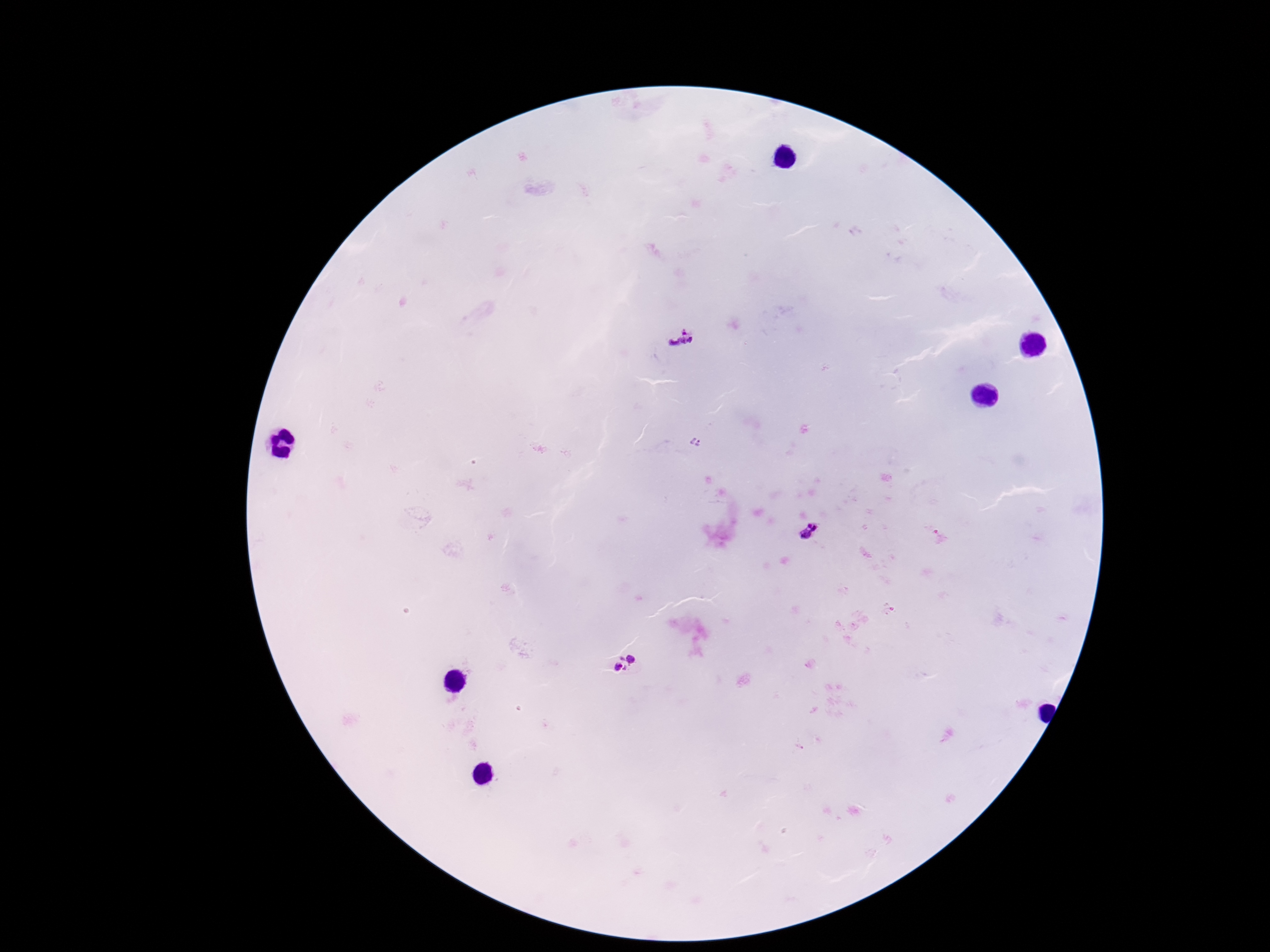

capture = smartphone camera through the microscope eyepiece
patient malaria status = positive
image size = 1270×952 pixels
magnification = 100x
field of view = one from this slide
Plasmodium parasite locations = approximate centers as {x, y} in pixels: {682, 337}, {695, 441}, {812, 531}, {626, 665}
stain = Giemsa
preparation = thick peripheral-blood smear